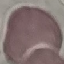

Summary:
  - Result: no malaria parasites detected
  - Image type: cell patch, automatically extracted from a larger field of view and resized to 64 × 64 pixels
  - Preparation: thin smear
  - Stain: Giemsa
  - Capture: smartphone through the microscope eyepiece